Give the position of every Plasmodium parasite visible.
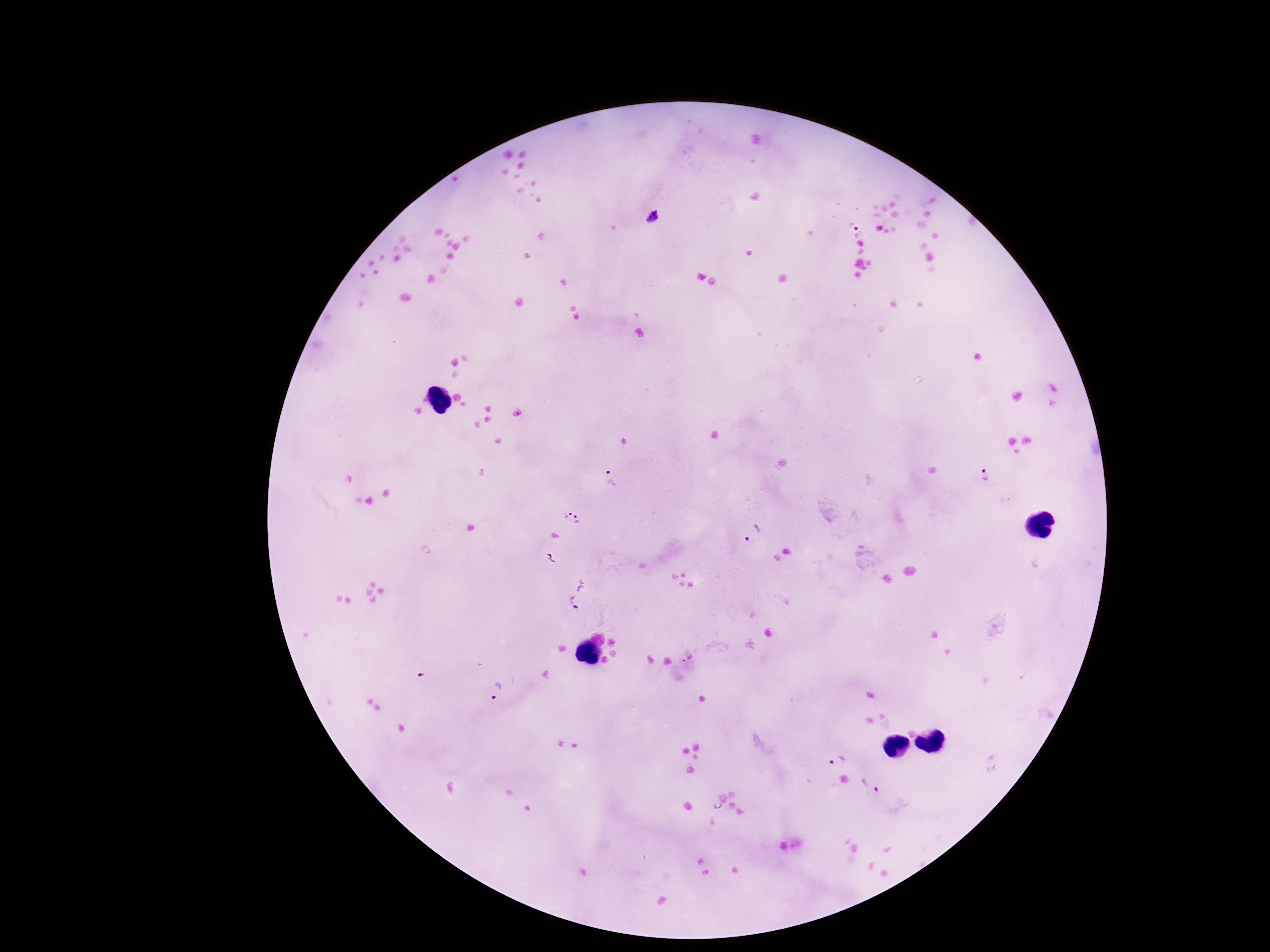

Approximate centers as [x, y] in pixels.
Plasmodium parasites: [654, 218], [853, 224], [985, 473], [610, 478], [566, 508], [579, 520], [753, 533], [576, 594], [687, 658], [495, 691], [835, 759], [870, 784].

Thick blood smear. 100x magnification. Giemsa-stained preparation. Single field of view. Photographed through the microscope eyepiece with a smartphone camera. Patient malaria status: infected. Image is 1270×952 pixels.